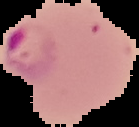
Summary:
  - Image size: 139×127 pixels
  - Image type: segmented cell region on a black background
  - Result: malaria parasites identified
  - Preparation: thin blood smear